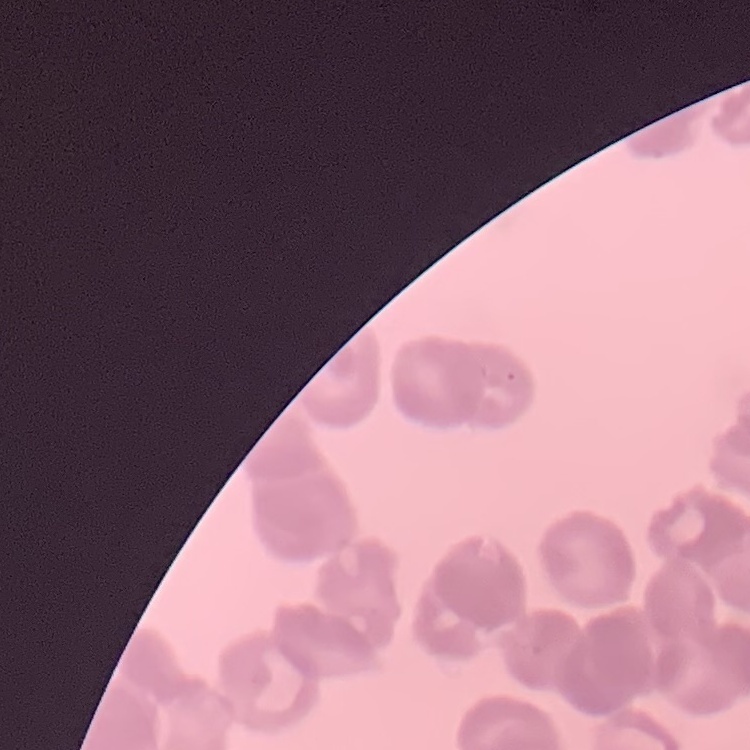 The erythrocytes exhibit rouleaux formation. One tile cut from a larger photomicrograph. Thin peripheral smear. Field's or Giemsa stain.